Identify the blood parasite species.
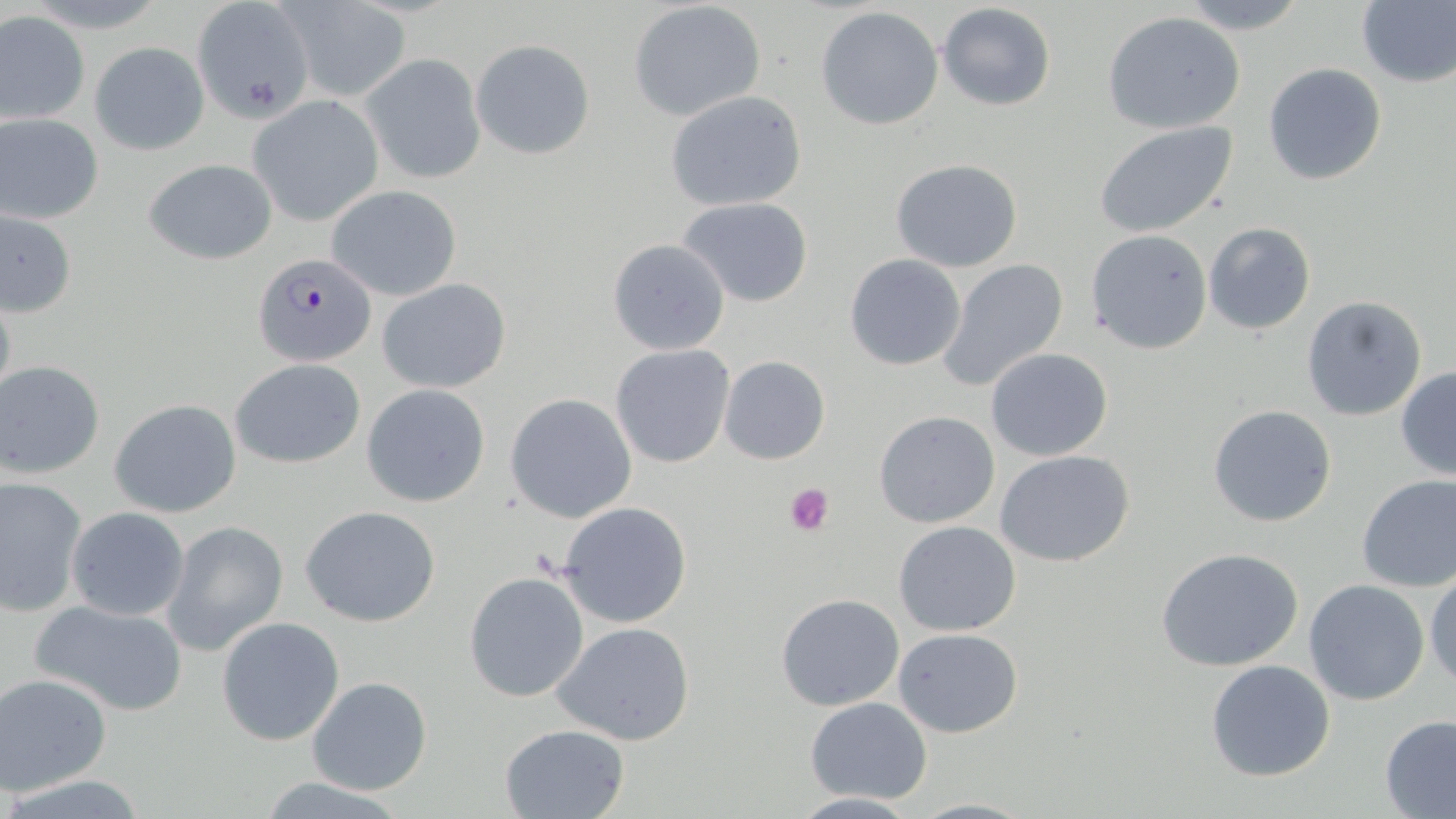

Plasmodium falciparum.

Approximate bounding boxes as [x1, y1, x2, y2] in pixels. Uninfected red blood cell locations: [190, 0, 313, 123], [627, 0, 766, 121], [1174, 0, 1309, 35], [1354, 0, 1456, 87], [282, 1, 411, 100], [936, 2, 1057, 112], [815, 8, 944, 130], [1102, 10, 1246, 134], [0, 11, 89, 125], [470, 39, 595, 161], [90, 41, 209, 155], [361, 54, 486, 185], [1263, 61, 1387, 185], [664, 90, 810, 211], [249, 95, 384, 227], [0, 112, 104, 224], [1094, 122, 1240, 240], [143, 158, 278, 264], [890, 158, 1024, 272], [324, 184, 462, 302], [679, 197, 813, 307], [0, 209, 77, 318], [1203, 221, 1316, 335], [1085, 230, 1214, 355], [607, 237, 731, 355], [844, 255, 966, 371], [937, 258, 1069, 391], [376, 277, 513, 394], [0, 286, 16, 410], [1301, 295, 1428, 422], [609, 343, 737, 468], [984, 347, 1113, 462], [718, 355, 831, 465], [231, 358, 367, 469], [0, 360, 106, 479], [1395, 366, 1456, 483], [361, 383, 491, 507], [504, 393, 636, 523], [109, 398, 242, 518], [1206, 404, 1337, 528], [875, 411, 1001, 528], [996, 450, 1135, 567], [1356, 474, 1456, 593], [1, 475, 89, 614], [557, 500, 694, 628], [300, 506, 443, 627], [65, 507, 189, 621], [160, 521, 289, 657], [894, 521, 1022, 636], [1156, 548, 1304, 673], [463, 570, 590, 703], [1425, 570, 1456, 691], [1303, 579, 1431, 705], [775, 592, 906, 712], [29, 598, 191, 717], [216, 617, 345, 745], [553, 621, 697, 746], [892, 627, 1023, 738], [1205, 660, 1336, 781], [1, 672, 112, 794], [306, 676, 434, 794], [804, 697, 932, 805], [1379, 714, 1456, 818], [498, 723, 630, 818], [0, 775, 157, 817], [252, 776, 419, 817], [789, 792, 925, 818], [909, 796, 1039, 818]. Plasmodium falciparum-infected red blood cell locations: [251, 254, 376, 367]. Platelet locations: [782, 481, 835, 539]. Image is 1456×819 pixels. Single field of view. Thin blood smear. Captured at 1000x magnification. May-Grünwald-Giemsa stain. Optical microscopy.